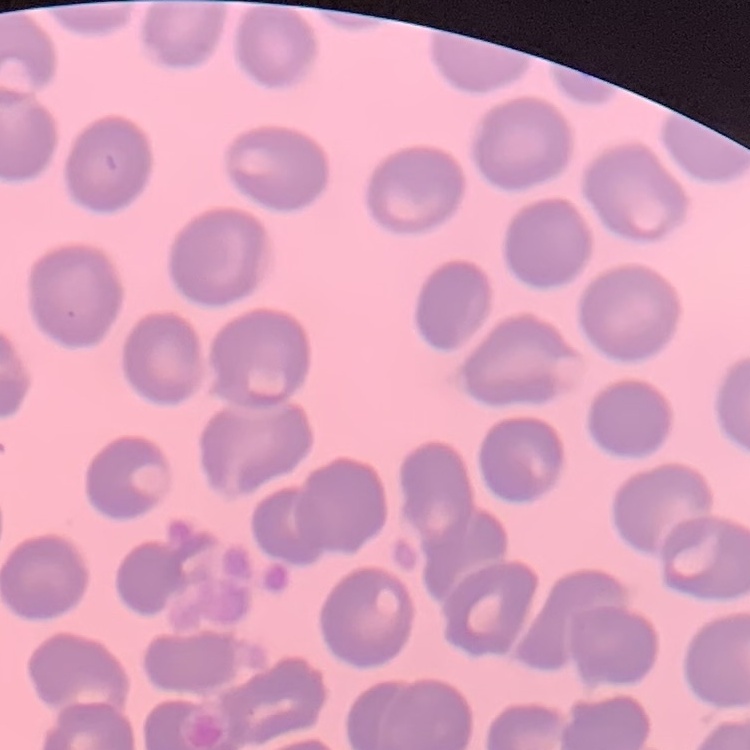
The red blood cells show no rouleaux formation. One tile cut from a larger photomicrograph. Thin blood film. Field's or Giemsa stain.